Report the malaria status of this cell.
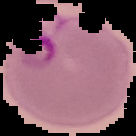

It is parasitized.

Image is 136×136 pixels. From a thin blood film. The area outside the segmented cell region is set to black.